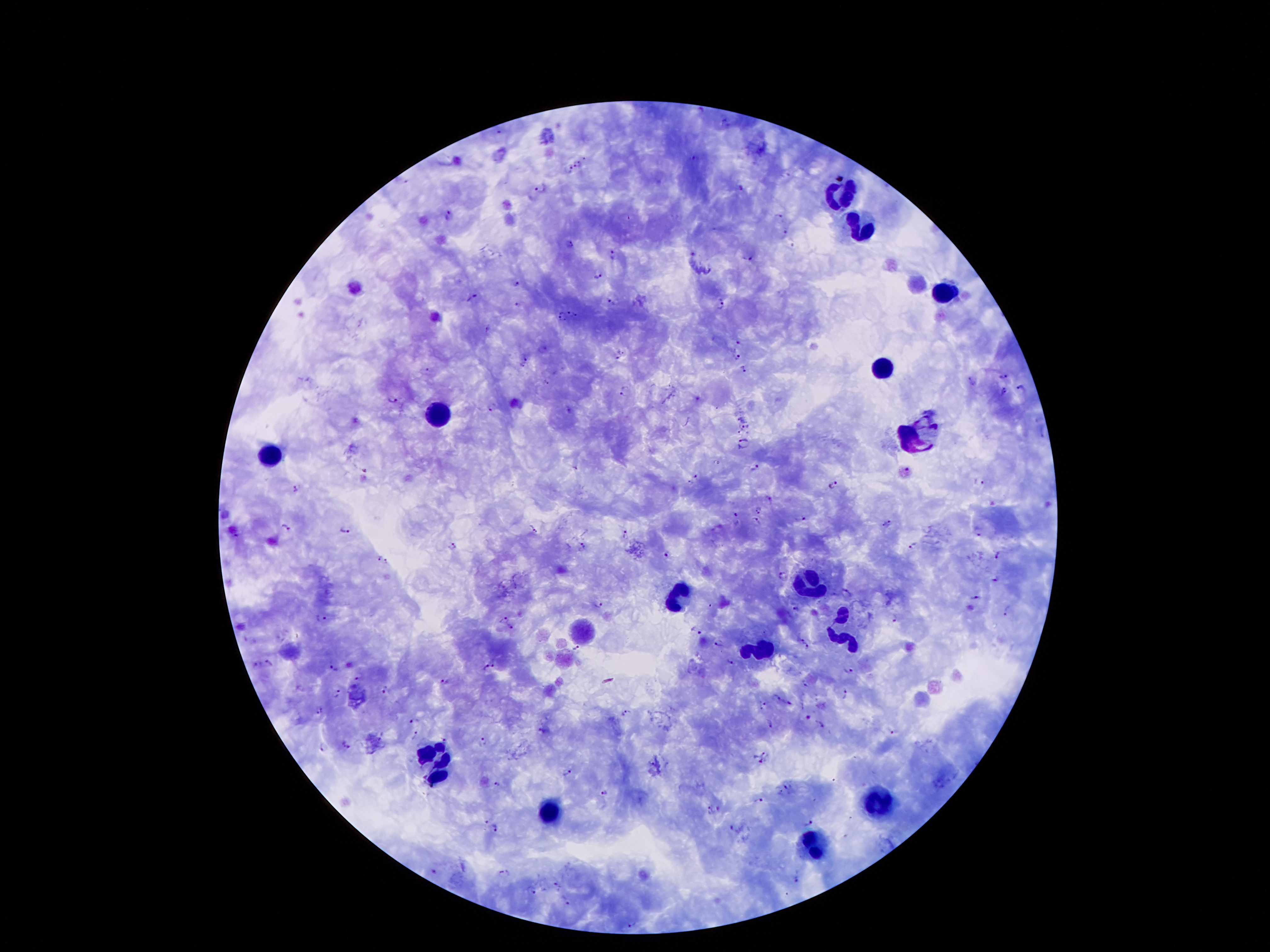

Approximate centers as (x, y) in pixels. Leukocyte locations: (836, 195), (860, 227), (948, 292), (883, 367), (435, 413), (920, 434), (274, 453), (811, 586), (677, 598), (841, 625), (757, 653), (437, 751), (438, 777), (876, 801), (550, 812), (814, 847). Malaria parasite locations: (579, 164), (568, 170), (402, 179), (540, 190), (742, 190), (449, 215), (779, 217), (785, 233), (571, 245), (793, 247), (615, 254), (750, 259), (597, 275), (517, 284), (473, 298), (611, 301), (721, 303), (518, 304), (567, 312), (577, 314), (562, 318), (487, 329), (741, 345), (544, 349), (623, 352), (737, 356), (524, 357), (617, 359), (522, 367), (743, 369), (428, 371), (1003, 376), (972, 381), (544, 383), (1020, 387), (1005, 390), (623, 393), (393, 398), (696, 398), (492, 409), (570, 412), (743, 426), (739, 432), (744, 444), (755, 467), (366, 470), (697, 477), (979, 482), (691, 483), (832, 484), (294, 488), (760, 510), (736, 515), (800, 517), (757, 521), (886, 523), (286, 527), (344, 530), (535, 530), (979, 531), (625, 534), (583, 543), (453, 545), (913, 545), (665, 553), (998, 555), (376, 556), (387, 562), (784, 576), (997, 580), (846, 593), (975, 598), (599, 604), (1007, 611), (794, 612), (895, 616), (322, 619), (504, 619), (510, 628), (698, 632), (798, 639), (718, 642), (808, 646), (576, 649), (730, 662), (256, 663), (269, 664), (496, 664), (332, 666), (486, 667), (849, 670), (359, 675), (443, 681), (805, 683), (384, 690), (335, 693), (846, 693), (777, 697), (790, 703), (762, 706), (319, 708), (626, 712), (807, 716), (413, 721), (772, 724), (821, 725), (541, 730), (893, 732), (415, 735), (483, 739), (443, 741), (346, 745), (325, 747), (765, 754), (757, 760), (565, 772), (496, 786), (787, 786), (780, 792), (603, 793), (758, 800), (719, 809), (709, 810), (485, 822), (808, 824), (496, 828), (733, 829), (434, 870), (503, 873), (797, 880), (556, 885), (532, 891), (569, 904), (632, 925). Photographed through the microscope eyepiece with a smartphone camera. Thick blood film. Patient malaria status: positive for Plasmodium falciparum. 100x magnification. Giemsa stain. Image is 1270×952 pixels. Single field of view.